Assess the morphology of the erythrocytes.
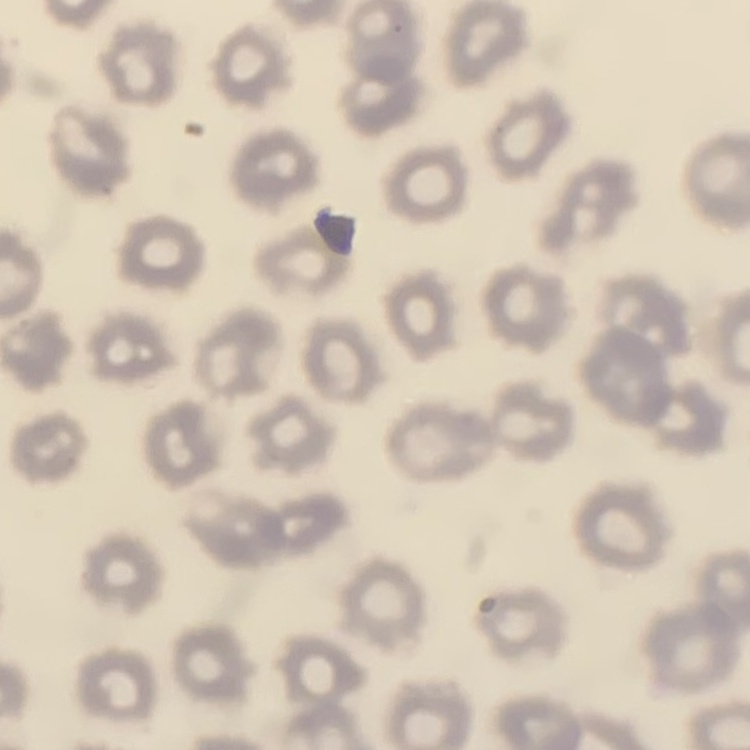

They show no rouleaux formation.

{
  "preparation": "thin blood smear",
  "stain": "Field's or Giemsa",
  "image_type": "square crop of a larger photomicrograph"
}